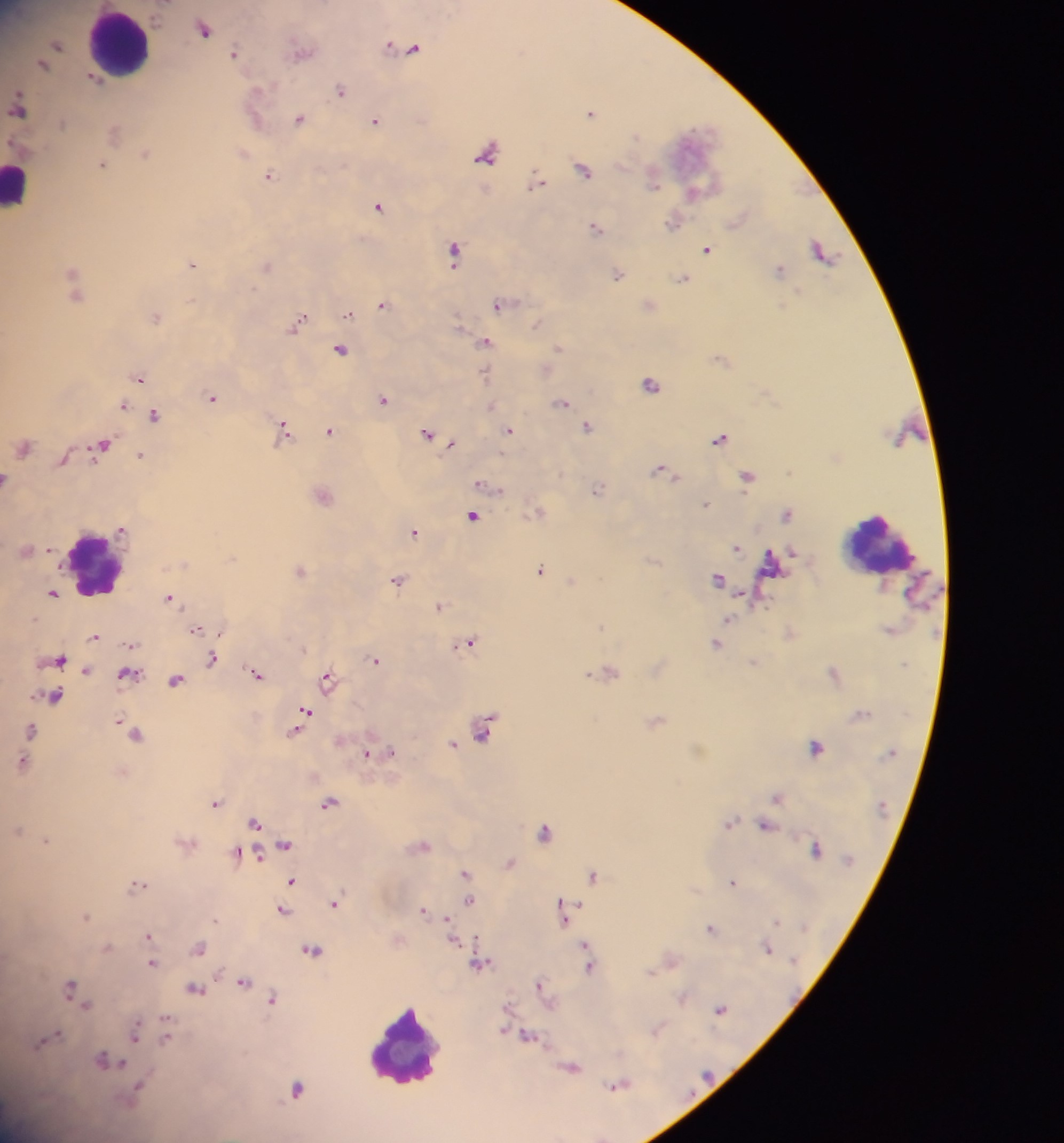

Approximate centers as [x, y] in pixels.
Summary:
  - Leukocyte locations: [122, 43], [18, 183], [879, 543], [95, 563], [404, 1048]
  - Plasmodium parasite locations: [204, 28], [58, 44], [399, 46], [412, 48], [303, 50], [235, 53], [43, 63], [95, 79], [342, 90], [19, 106], [591, 111], [301, 118], [375, 121], [115, 132], [489, 152], [146, 153], [243, 153], [103, 164], [585, 169], [271, 176], [653, 176], [538, 181], [695, 192], [380, 206], [674, 221], [597, 227], [707, 249], [455, 251], [822, 251], [193, 264], [267, 265], [780, 268], [618, 274], [683, 278], [74, 280], [501, 304], [383, 305], [650, 305], [350, 313], [156, 316], [298, 322], [537, 323], [487, 342], [343, 348], [559, 348], [546, 369], [485, 374], [140, 378], [652, 384], [214, 397], [385, 399], [563, 403], [124, 405], [490, 406], [156, 415], [588, 426], [286, 429], [510, 430], [330, 431], [427, 433], [722, 439], [452, 443], [103, 444], [25, 446], [142, 456], [64, 458], [666, 471], [749, 476], [7, 478], [482, 484], [598, 490], [323, 494], [706, 503], [539, 511], [787, 513], [474, 516], [124, 530], [415, 531], [737, 547], [28, 550], [541, 568], [301, 569], [719, 578], [399, 580], [573, 581], [53, 593], [170, 597], [441, 605], [729, 619], [197, 629], [222, 632], [95, 636], [469, 642], [717, 643], [132, 644], [60, 659], [212, 659], [377, 659], [756, 662], [87, 670], [609, 670], [834, 672], [129, 673], [257, 674], [329, 678], [176, 680], [55, 696], [306, 710], [657, 720], [485, 728], [32, 729], [295, 732], [135, 733], [453, 744], [817, 746], [393, 751], [367, 753], [25, 762], [778, 796], [217, 802], [330, 804], [256, 822], [730, 822], [766, 826], [18, 830], [546, 831], [47, 840], [286, 844], [423, 846], [817, 849], [241, 854], [257, 854], [511, 862], [466, 872], [594, 875], [292, 881], [734, 881], [140, 884], [471, 900], [336, 902], [424, 910], [284, 911], [566, 912], [86, 917], [448, 919], [711, 927], [150, 935], [454, 938], [108, 946], [201, 947], [767, 947], [313, 950], [587, 950], [671, 959], [153, 963], [480, 963], [591, 965], [244, 981], [542, 983], [74, 989], [196, 989], [683, 997], [274, 999], [85, 1000], [721, 1009], [658, 1029], [136, 1032], [166, 1033], [528, 1035], [45, 1041], [108, 1059], [572, 1067], [620, 1084], [298, 1087], [138, 1088]
  - Country: Ghana
  - Field of view: single
  - Image size: 1064×1143 pixels
  - Capture: mobile-phone photograph through a microscope
  - Preparation: thick blood film